Report the malaria status of this cell.
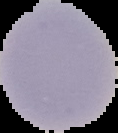
Uninfected.

preparation = thin blood film
image type = segmented cell region with the area outside set to black
image size = 118×133 pixels